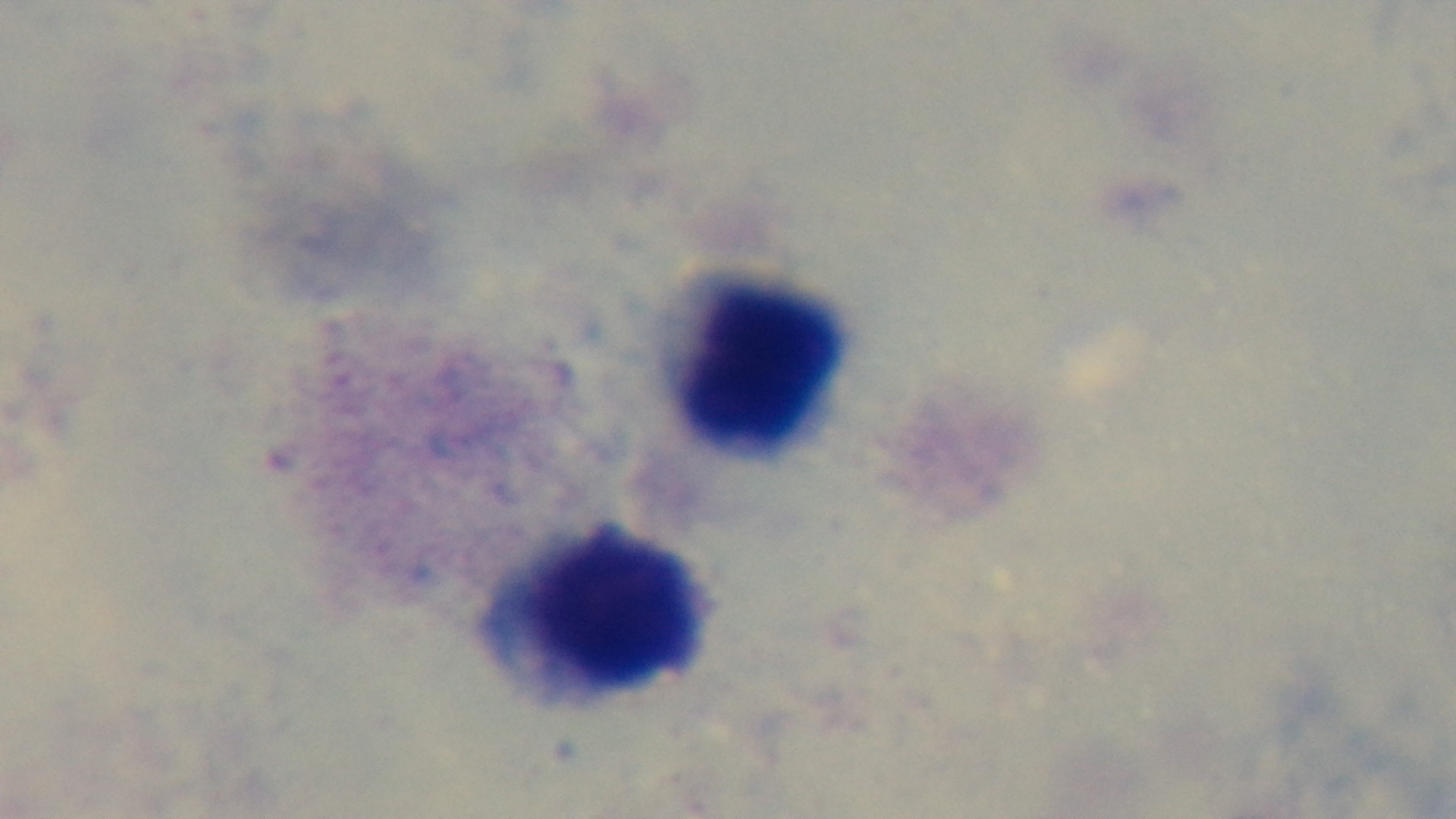
Summary:
  - Modality: light microscopy
  - Capture: mounted 4K digital camera
  - Preparation: thick smear
  - Malaria status: negative
  - Objective: 100x oil immersion
  - Field of view: single
  - Stain: Giemsa